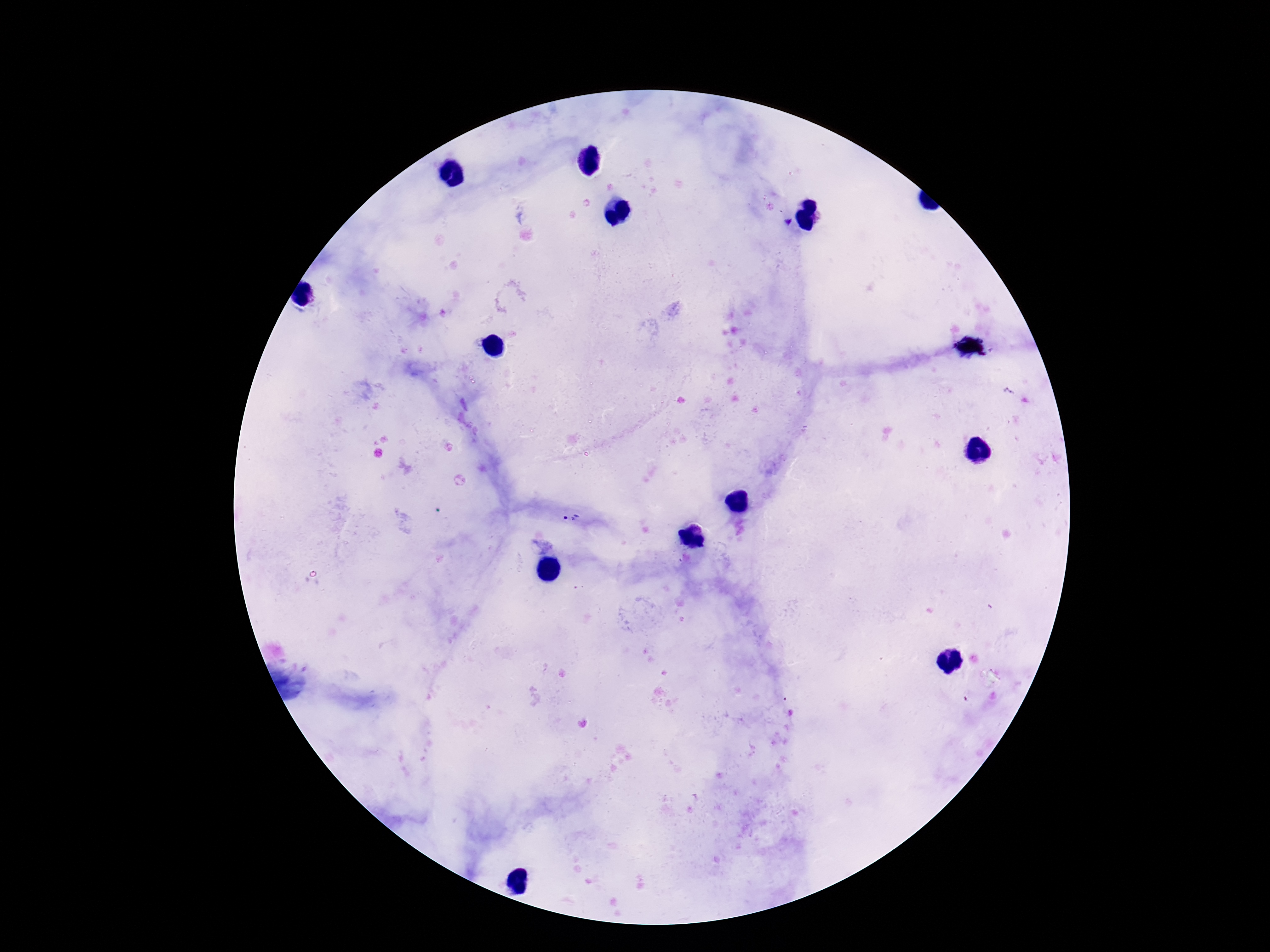
Approximate object centers, in pixels from the top-left corner.
Summary:
  - Plasmodium parasite locations: (x=571, y=518)
  - Preparation: thick peripheral-blood smear
  - Image size: 1270×952 pixels
  - Patient malaria status: infected
  - Field of view: one from this slide
  - Capture: smartphone camera through the microscope eyepiece
  - Magnification: 100x
  - Stain: Giemsa